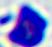

{
  "magnification": "400x",
  "identification": "white blood cell",
  "modality": "photomicrograph"
}